Report the malaria status of this cell.
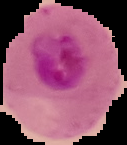
Parasitized.

Summary:
  - Preparation: thin blood smear
  - Image size: 127×145 pixels
  - Image type: segmented cell region on a black background